Assess this cell for malaria.
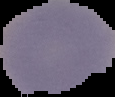
Uninfected.

preparation = thin blood smear
image type = segmented cell region on a black background
image size = 115×97 pixels